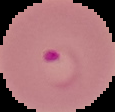
Summary:
  - Image size: 115×112 pixels
  - Image type: cell region segmented out of the field of view; surrounding area masked to black
  - Preparation: thin blood smear
  - Result: malaria parasites detected